State the preparation type.
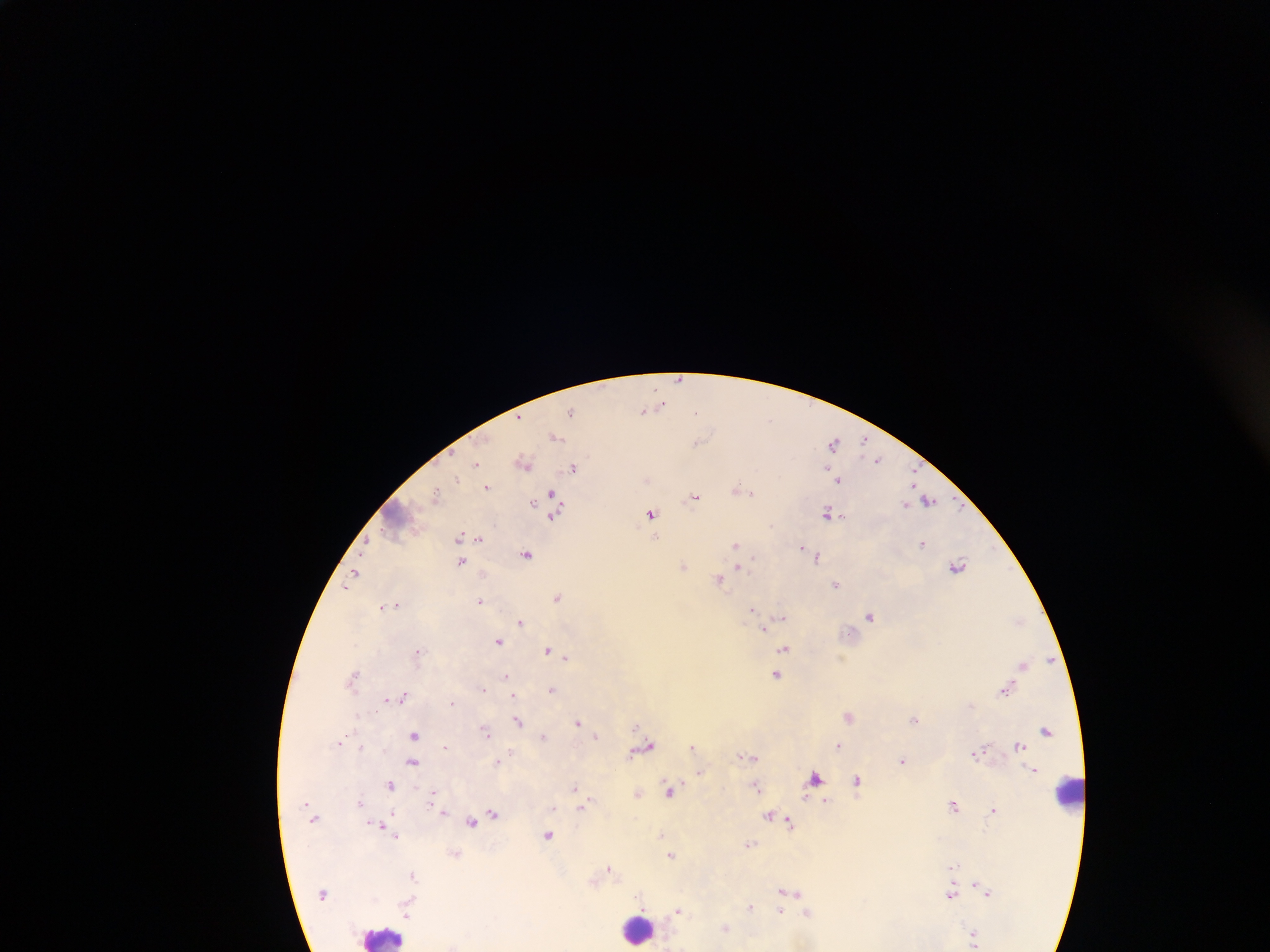

Thick blood smear.

field of view = single
Plasmodium parasite locations = approximate centers as (x, y) in pixels: (680, 379), (662, 402), (645, 410), (571, 411), (556, 436), (698, 441), (865, 441), (834, 443), (878, 459), (524, 462), (476, 463), (575, 467), (455, 479), (838, 479), (487, 487), (741, 490), (436, 494), (696, 497), (555, 500), (926, 500), (534, 502), (556, 510), (651, 513), (828, 513), (461, 537), (655, 537), (478, 538), (367, 541), (923, 543), (736, 545), (804, 548), (809, 552), (527, 553), (817, 556), (461, 561), (683, 565), (957, 565), (738, 568), (353, 577), (719, 579), (837, 584), (558, 596), (481, 601), (385, 606), (393, 606), (753, 609), (871, 615), (783, 616), (1019, 619), (522, 621), (764, 628), (767, 632), (499, 640), (784, 648), (548, 650), (418, 651), (566, 657), (1051, 659), (1023, 664), (777, 674), (505, 677), (354, 678), (483, 688), (1006, 688), (552, 689), (513, 695), (403, 696), (393, 699), (386, 700), (452, 702), (849, 715), (915, 718), (519, 720), (578, 723), (485, 730), (1046, 730), (414, 734), (543, 736), (597, 736), (340, 743), (838, 745), (692, 746), (1019, 746), (362, 747), (446, 747), (644, 747), (979, 752), (750, 755), (902, 760), (414, 761), (497, 761), (1034, 769), (701, 771), (815, 777), (857, 780), (391, 784), (757, 787), (575, 788), (671, 789), (433, 790), (638, 793), (807, 797), (823, 799), (592, 800), (587, 802), (360, 803), (954, 805), (582, 806), (993, 809), (444, 811), (393, 812), (493, 812), (771, 815), (475, 819), (472, 821), (378, 822), (790, 822), (661, 834), (549, 835), (396, 836), (750, 844), (455, 852), (671, 855), (951, 867), (609, 868), (415, 876), (973, 883), (793, 891), (988, 892), (952, 893), (640, 895), (409, 902), (751, 907), (678, 910), (781, 910), (808, 914), (410, 915), (725, 928), (974, 934)
image size = 1270×952 pixels
country = Ghana
leukocyte locations = approximate centers as (x, y) in pixels: (1067, 791), (639, 929), (385, 935)
capture = mobile-phone photograph through a microscope